Classify this cell by malaria status.
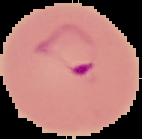
It is parasitized.

Summary:
  - Image size: 142×139 pixels
  - Preparation: thin blood film
  - Image type: segmented cell region on a black background